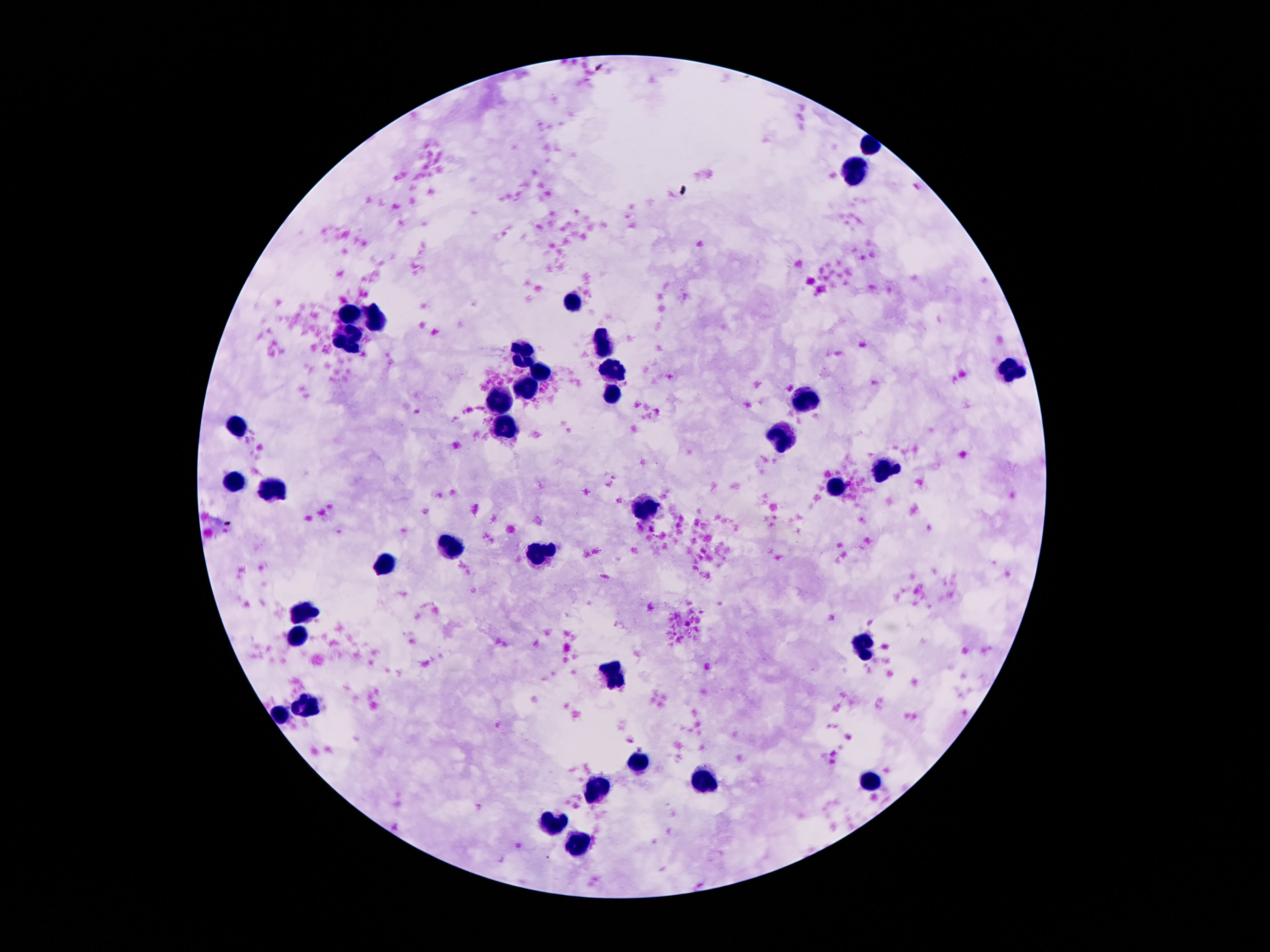
stain: Giemsa
leukocyte_locations: 'approximate centers as [x, y] in pixels: [853, 168], [570, 302], [353, 313], [376, 320], [351, 339], [605, 343], [524, 349], [1011, 369], [614, 370], [540, 372], [526, 388], [612, 395], [806, 400], [502, 402], [505, 423], [241, 426], [782, 438], [887, 466], [234, 483], [276, 488], [841, 488], [645, 511], [453, 547], [537, 555], [383, 567], [307, 612], [295, 640], [866, 644], [612, 677], [307, 701], [281, 713], [640, 761], [871, 782], [706, 783], [598, 789], [556, 823], [580, 848]'
field_of_view: single
magnification: 100x
patient_malaria_status: negative
preparation: thick blood film
capture: smartphone camera through the microscope eyepiece
image_size: 1270×952 pixels